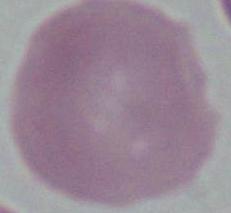
magnification: 1000x
identification: erythrocyte
modality: micrograph